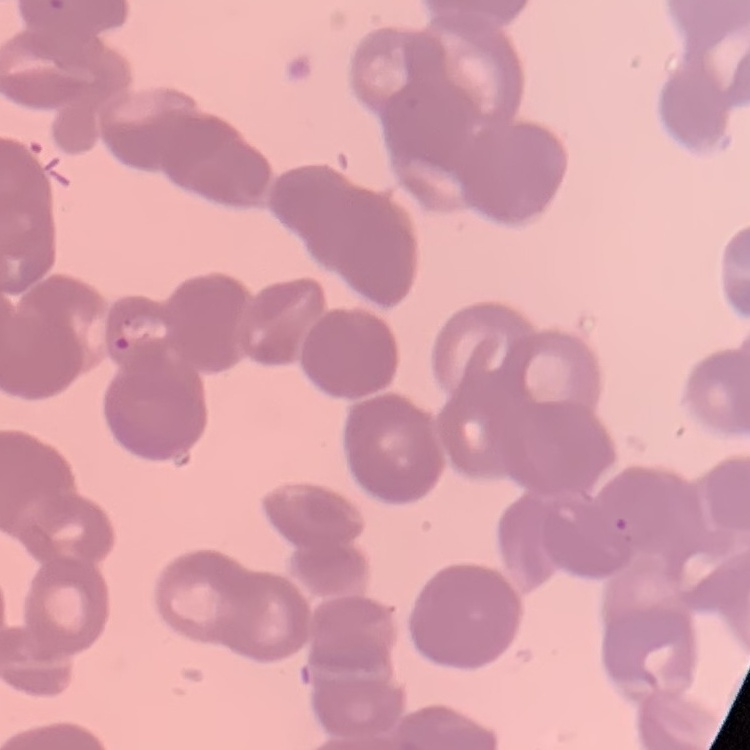

red blood cell morphology = rouleaux formation
image type = square crop of a larger photomicrograph
preparation = thin peripheral smear
stain = Field's or Giemsa